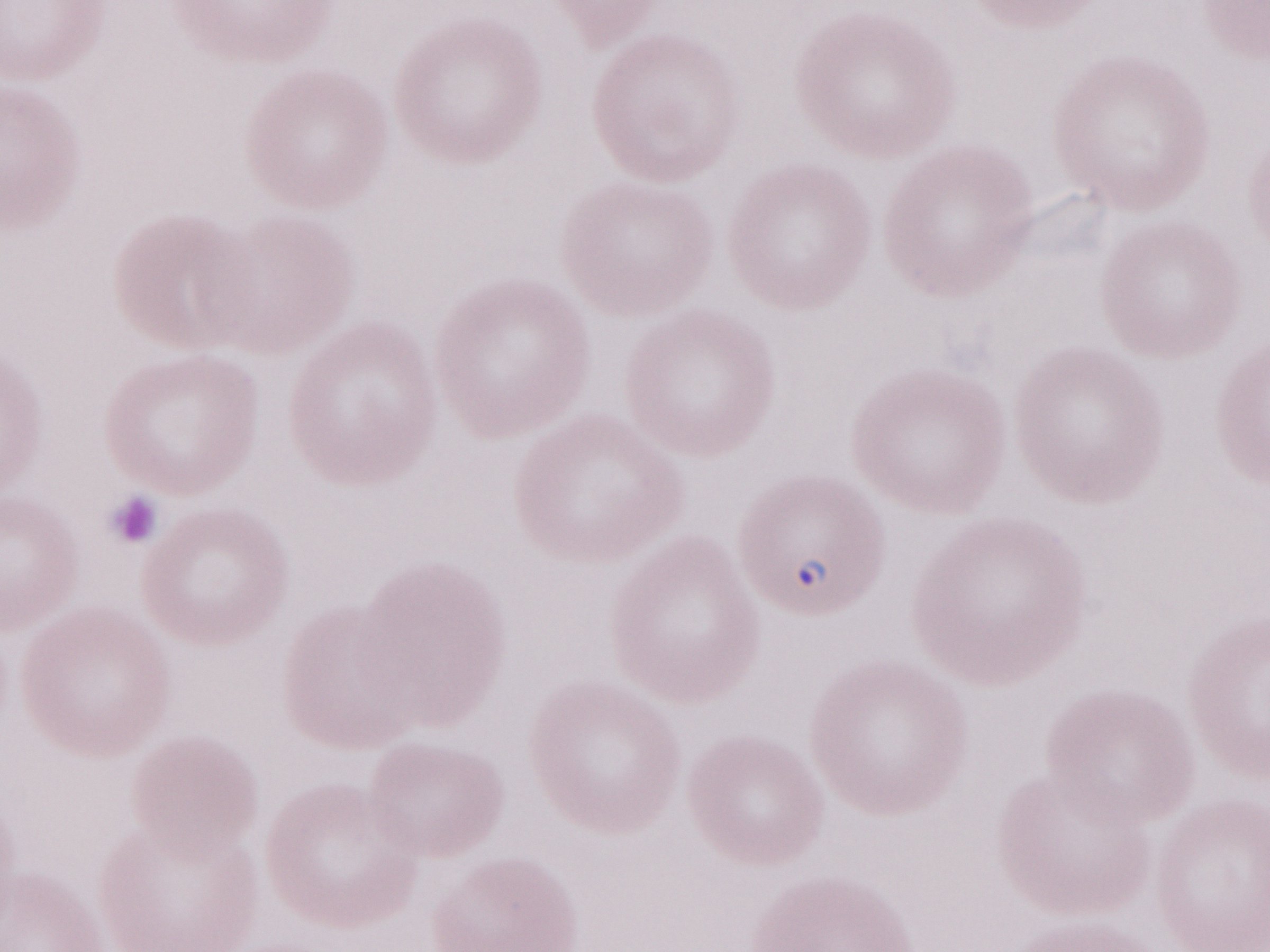

Image is 1270×952 pixels. Olympus BX43 microscope and DP73 digital camera. Malaria diagnosis (patient-level): positive. Magnification: 1,000x. One field of this slide. Thin peripheral-blood smear. May-Grünwald-Giemsa stain.